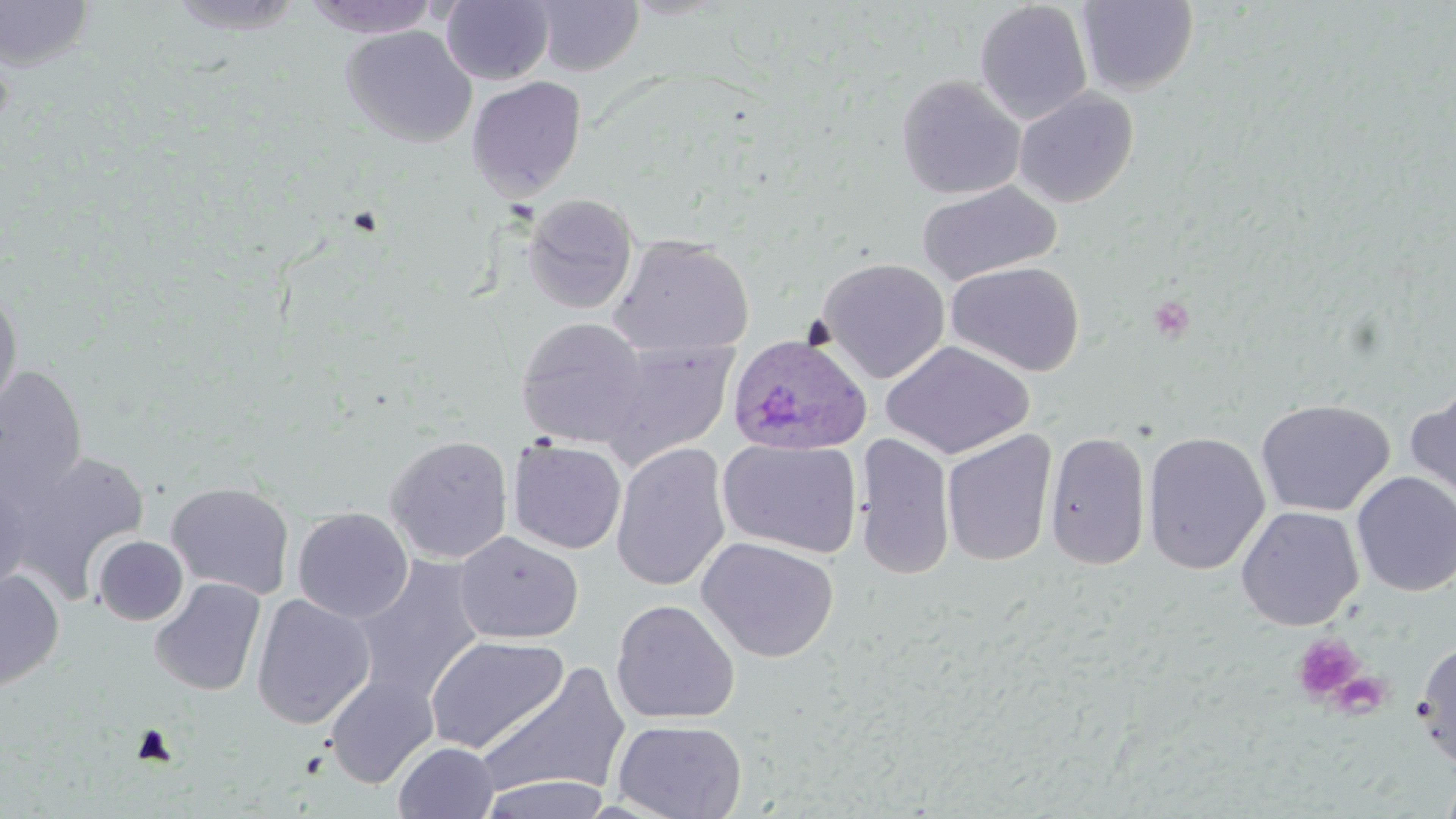

Summary:
  - Coordinate format: approximate bounding boxes as (x1, y1, x2, y2) in pixels
  - Platelet locations: (1291, 633, 1365, 704), (1338, 676, 1385, 723)
  - Uninfected red blood cell locations: (163, 0, 309, 36), (303, 0, 441, 38), (532, 0, 644, 76), (0, 1, 96, 71), (441, 1, 554, 85), (973, 1, 1093, 125), (1075, 1, 1199, 95), (341, 25, 477, 147), (466, 75, 587, 201), (896, 75, 1025, 199), (1013, 88, 1138, 207), (916, 180, 1062, 287), (520, 193, 639, 315), (608, 234, 756, 359), (817, 257, 950, 383), (946, 261, 1085, 377), (0, 288, 24, 419), (515, 317, 651, 448), (596, 340, 739, 469), (881, 340, 1035, 460), (0, 366, 88, 501), (1404, 387, 1456, 517), (1256, 399, 1395, 517), (941, 429, 1057, 567), (1044, 431, 1151, 571), (1142, 431, 1270, 575), (854, 432, 955, 580), (385, 434, 513, 564), (718, 438, 863, 558), (508, 439, 627, 554), (611, 442, 731, 593), (8, 449, 151, 600), (1351, 471, 1456, 597), (0, 476, 33, 599), (165, 481, 295, 600), (1235, 505, 1364, 631), (292, 507, 414, 623), (454, 531, 584, 645), (93, 535, 188, 626), (697, 536, 839, 663), (351, 555, 486, 707), (0, 570, 65, 693), (149, 577, 266, 697), (250, 594, 376, 729), (610, 599, 740, 725), (424, 635, 569, 754), (1414, 639, 1456, 769), (475, 663, 633, 802), (324, 673, 439, 788), (612, 718, 747, 819), (393, 741, 498, 819), (1438, 765, 1456, 819), (477, 774, 612, 818)
  - Plasmodium ovale-infected red blood cell locations: (727, 333, 871, 455)
  - Slide-level diagnosis: Plasmodium ovale
  - Field of view: single
  - Modality: light microscopy
  - Stain: May-Grünwald-Giemsa
  - Image size: 1456×819 pixels
  - Preparation: thin blood film
  - Magnification: 1000x